Outline every malaria parasite, every leukocyte, and every artifact (stain precipitate or debris).
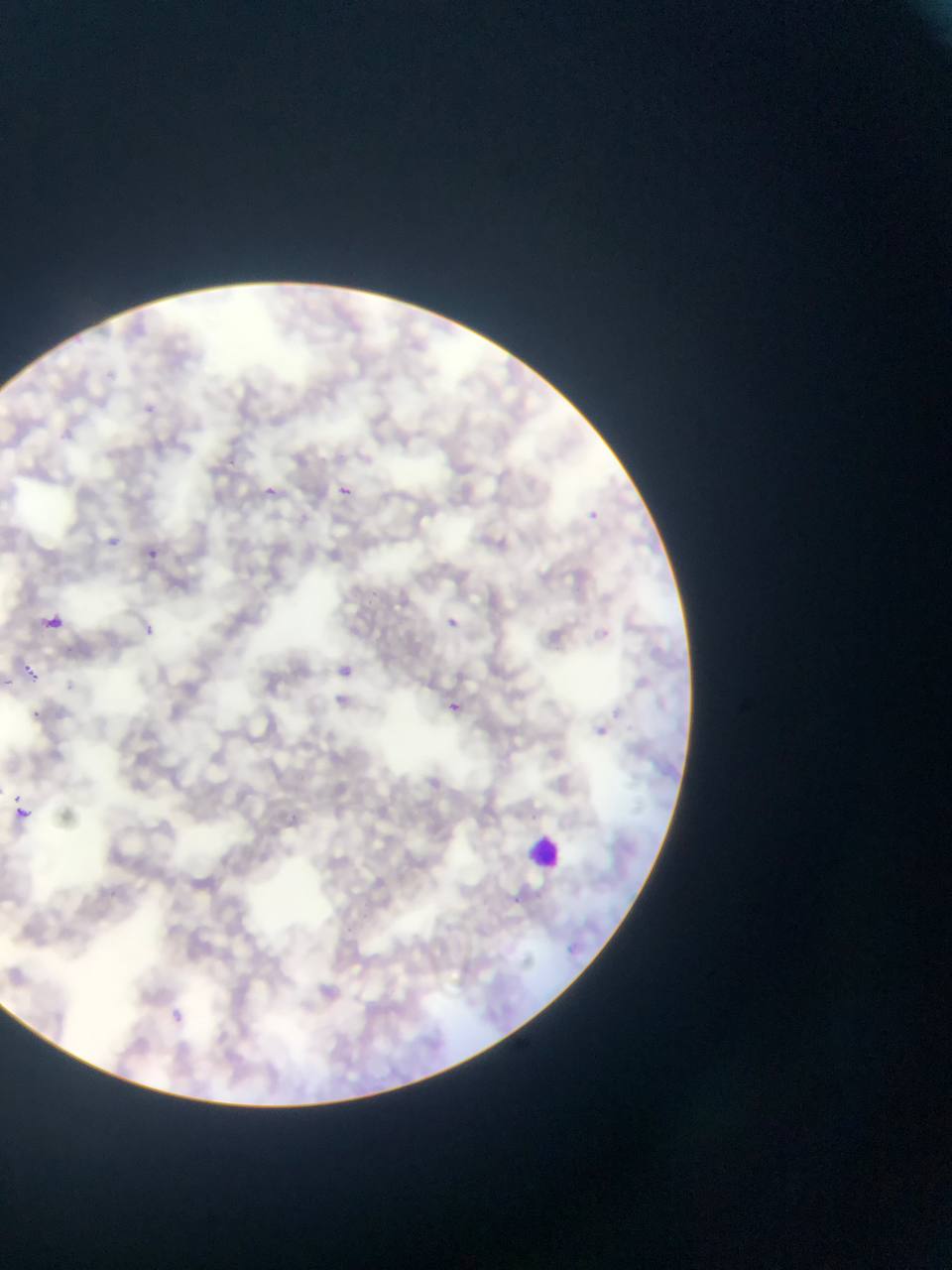
Approximate bounding boxes as {left, top, right, bottom} in pixels.
Malaria parasites: {335, 483, 354, 501}, {262, 484, 284, 504}, {580, 506, 604, 528}, {108, 534, 124, 555}, {144, 549, 158, 564}, {43, 612, 65, 632}, {443, 613, 462, 631}, {133, 620, 160, 643}, {334, 661, 356, 682}, {442, 698, 466, 720}, {25, 707, 45, 726}, {592, 714, 618, 745}, {10, 805, 33, 827}, {310, 977, 353, 1016}.
Leukocytes: {525, 830, 568, 874}.

Single field of view. Thin blood film. Image is 952×1270 pixels. Sample from Ghana. Photographed through a microscope with a mobile-phone camera.